Locate and identify every blood parasite.
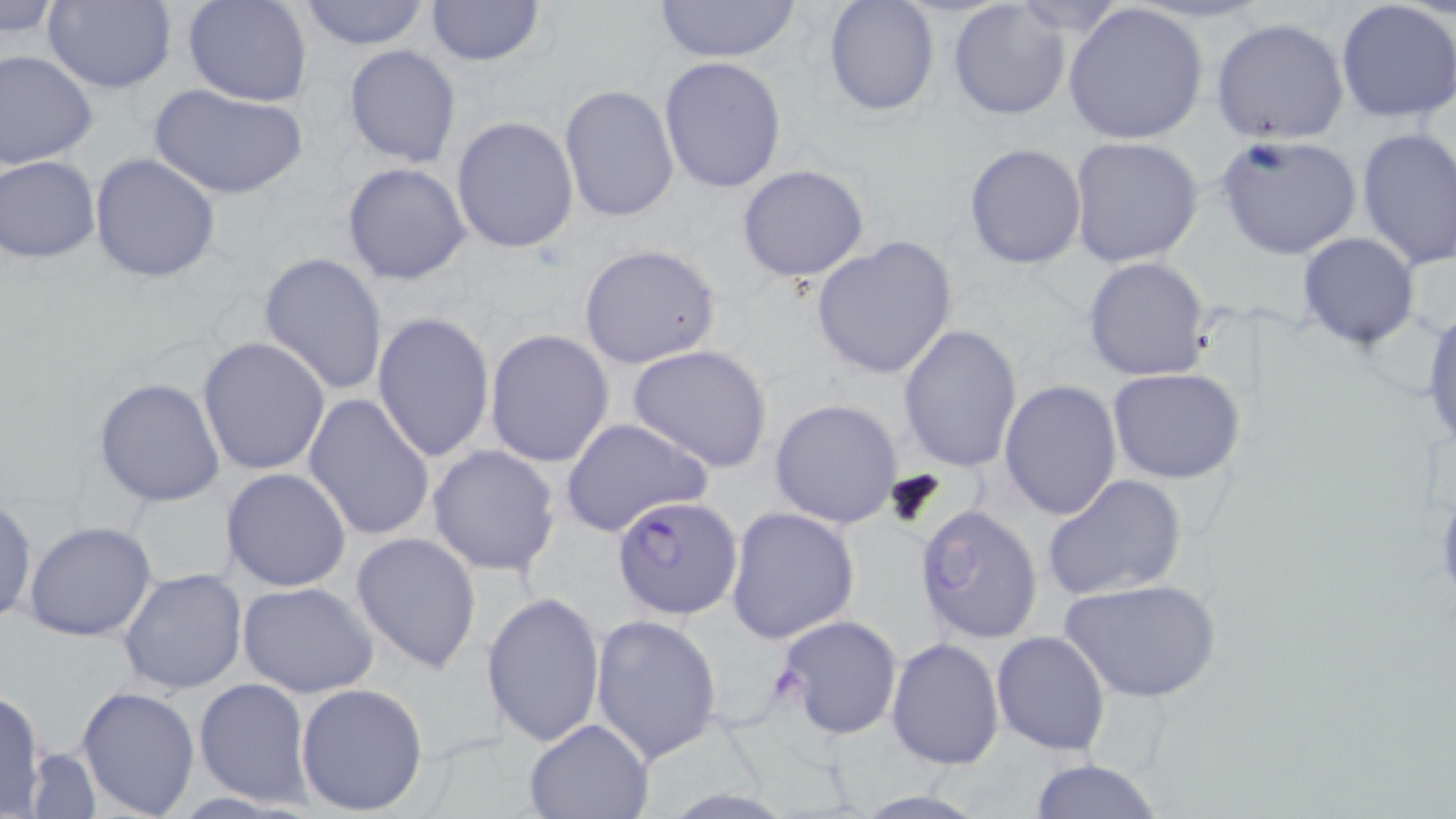
Approximate bounding boxes as (x1,y1)-(x2,y2) corner pairs in pixels.
Plasmodium falciparum-infected red blood cells: (612,495)-(745,619).
No Plasmodium ovale, Plasmodium malariae, Plasmodium vivax, Babesia divergens, or Trypanosoma brucei observed.

slide-level diagnosis = Plasmodium falciparum
stain = May-Grünwald-Giemsa
image size = 1456×819 pixels
field of view = one of a larger specimen
uninfected red blood cell locations = approximate bounding boxes as (x1,y1)-(x2,y2) corner pairs in pixels: (43,0)-(178,94), (182,0)-(313,106), (296,0)-(431,50), (422,0)-(548,69), (650,0)-(804,62), (822,0)-(940,118), (0,1)-(64,42), (948,1)-(1072,119), (1062,1)-(1210,146), (1335,1)-(1456,122), (1210,16)-(1351,146), (343,44)-(461,168), (0,50)-(98,169), (658,56)-(787,194), (558,83)-(679,223), (152,85)-(305,201), (450,115)-(580,255), (1356,127)-(1456,271), (1217,132)-(1364,261), (1068,136)-(1204,269), (963,143)-(1087,268), (89,153)-(221,282), (1,155)-(100,263), (341,162)-(472,285), (735,163)-(870,284), (1298,232)-(1421,348), (810,237)-(959,380), (579,243)-(724,370), (257,252)-(388,397), (1082,256)-(1212,382), (1422,305)-(1456,458), (371,309)-(494,463), (897,323)-(1022,473), (485,329)-(615,468), (198,336)-(331,474), (626,344)-(774,473), (1107,368)-(1246,483), (93,377)-(226,507), (999,380)-(1123,521), (302,391)-(437,544), (770,399)-(902,530), (560,417)-(713,536), (427,444)-(563,576), (221,468)-(352,593), (1042,474)-(1187,603), (0,497)-(38,627), (912,504)-(1044,645), (724,505)-(860,644), (24,521)-(158,642), (351,531)-(482,673), (118,566)-(249,697), (1060,577)-(1220,703), (238,581)-(380,698), (480,592)-(605,750), (774,613)-(904,741), (591,614)-(724,767), (991,631)-(1110,756), (886,637)-(1005,769), (194,678)-(315,809), (295,681)-(429,815), (77,683)-(200,816), (0,688)-(50,816), (523,717)-(655,819), (25,745)-(100,817), (1027,759)-(1165,818)
magnification = 1000x
modality = light microscopy
preparation = thin blood smear